Draw a bounding box around every Plasmodium parasite.
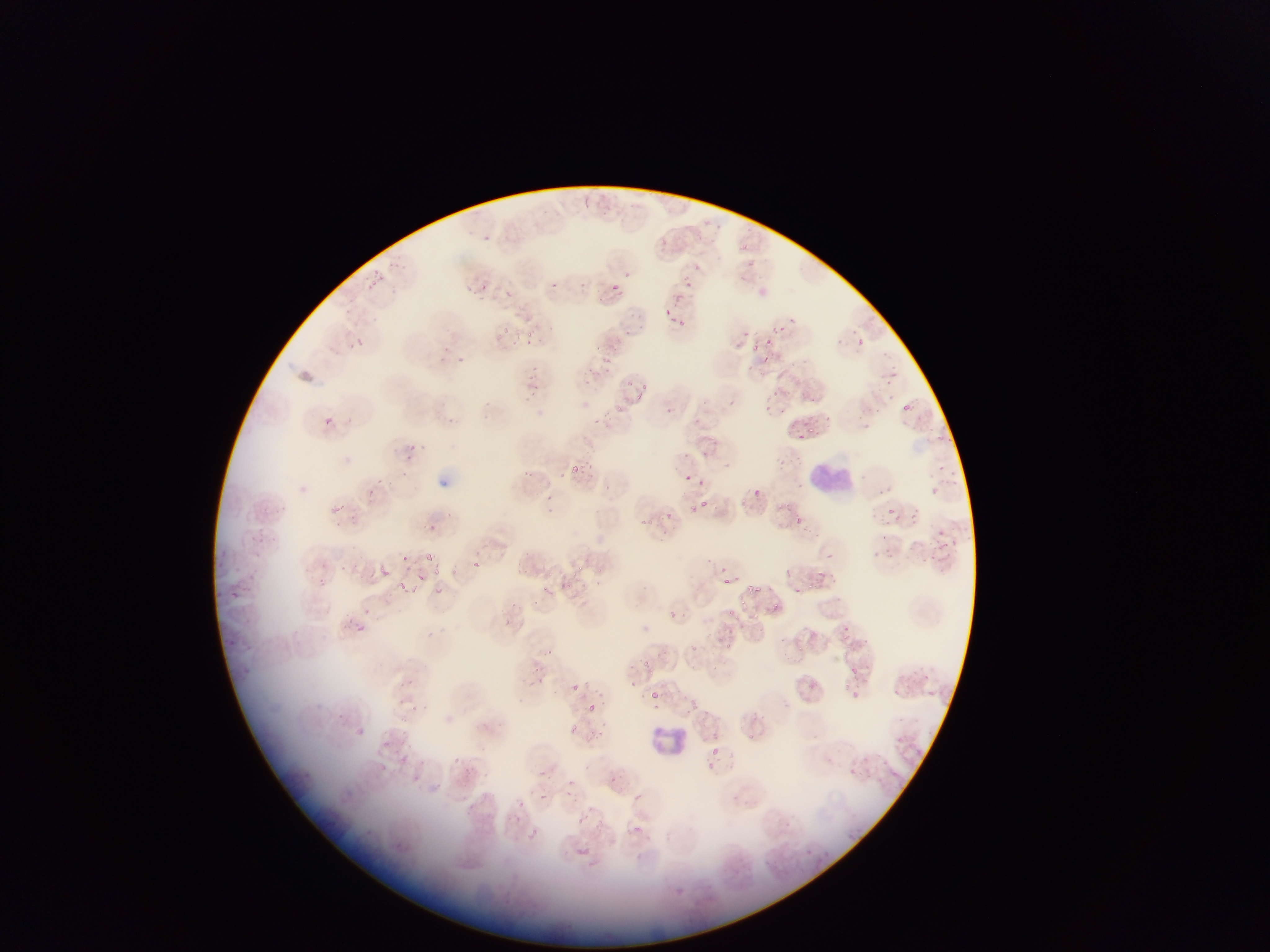
Approximate bounding boxes as (left, top, right, bottom) in pixels.
Plasmodium parasites (some below the resolvable threshold): (658, 237, 671, 251), (740, 241, 747, 253), (696, 261, 705, 270), (373, 271, 380, 281), (687, 280, 693, 288), (368, 281, 373, 290), (482, 281, 486, 290), (609, 283, 621, 294), (679, 292, 685, 301), (667, 308, 673, 318), (678, 318, 686, 330), (772, 325, 780, 332), (781, 325, 789, 333), (503, 326, 516, 334), (625, 328, 631, 336), (528, 331, 537, 337), (351, 337, 364, 349), (855, 338, 864, 346), (524, 340, 529, 348), (754, 343, 762, 351), (598, 345, 604, 354), (764, 354, 769, 363), (602, 357, 611, 362), (803, 358, 811, 373), (750, 363, 757, 375), (639, 381, 649, 390), (774, 390, 782, 398), (530, 392, 538, 402), (637, 392, 646, 400), (730, 398, 736, 407), (616, 406, 628, 413), (321, 416, 335, 428), (594, 417, 602, 426), (695, 418, 703, 423), (809, 427, 820, 436), (794, 433, 807, 442), (405, 444, 418, 457), (722, 458, 730, 469), (581, 461, 596, 467), (569, 464, 578, 477), (939, 465, 945, 474), (525, 470, 533, 478), (950, 470, 958, 475), (561, 471, 568, 480), (685, 474, 691, 483), (379, 478, 390, 485), (931, 485, 939, 495), (756, 486, 762, 496), (702, 499, 708, 509), (688, 502, 697, 512), (332, 505, 340, 511), (887, 506, 894, 516), (664, 510, 672, 519), (910, 512, 917, 520), (639, 515, 645, 524), (647, 517, 655, 524), (793, 517, 802, 522), (430, 522, 440, 531), (882, 533, 889, 542), (951, 538, 961, 548), (939, 542, 948, 552), (884, 551, 897, 561), (925, 552, 935, 563), (828, 553, 834, 562), (403, 555, 412, 564), (472, 560, 483, 570), (341, 563, 350, 572), (578, 563, 586, 573), (380, 565, 400, 585), (432, 565, 440, 579), (720, 565, 728, 570), (520, 567, 529, 575), (818, 569, 826, 578), (418, 572, 426, 583), (724, 577, 737, 587), (556, 578, 573, 592), (597, 579, 602, 591), (397, 580, 418, 598), (808, 581, 818, 588), (572, 582, 588, 588), (746, 584, 756, 594), (755, 584, 764, 593), (432, 586, 438, 595), (543, 586, 552, 594), (231, 590, 243, 600), (533, 599, 541, 608), (728, 607, 738, 617), (667, 608, 679, 622), (359, 624, 367, 632), (429, 627, 435, 642), (844, 634, 853, 643), (228, 638, 236, 648), (690, 641, 705, 658), (801, 646, 811, 655), (644, 657, 656, 667), (851, 667, 861, 678), (919, 667, 932, 682), (407, 674, 413, 685), (912, 677, 921, 688), (570, 683, 580, 693), (891, 686, 899, 698), (650, 690, 661, 700), (852, 690, 863, 697), (692, 695, 703, 710), (399, 696, 406, 709), (588, 702, 603, 714), (413, 704, 421, 711), (655, 705, 664, 710), (760, 715, 766, 725), (567, 723, 581, 735), (354, 725, 365, 738), (595, 727, 611, 742), (747, 731, 754, 739), (711, 748, 718, 758), (452, 756, 463, 769), (849, 766, 860, 774), (540, 769, 551, 780), (569, 772, 575, 785), (612, 772, 619, 787), (564, 786, 575, 799), (540, 792, 551, 801), (469, 803, 475, 814), (579, 813, 588, 829), (515, 815, 523, 823), (532, 825, 539, 833), (631, 825, 646, 835) | approximate (x, y) pixel centers of objects too small to bound: (556, 285), (790, 318), (747, 333), (769, 341), (533, 375), (536, 388), (905, 406), (667, 409), (405, 473), (702, 482), (889, 489), (373, 490), (549, 498), (429, 554), (321, 579), (796, 590), (743, 602), (774, 604), (709, 767), (521, 802).

Summary:
  - Leukocyte locations: (809, 457, 857, 503), (652, 726, 684, 757)
  - Capture: mobile-phone photograph through a microscope
  - Field of view: single
  - Preparation: thin blood smear
  - Image size: 1270×952 pixels
  - Country: Ghana